Locate every Plasmodium parasite.
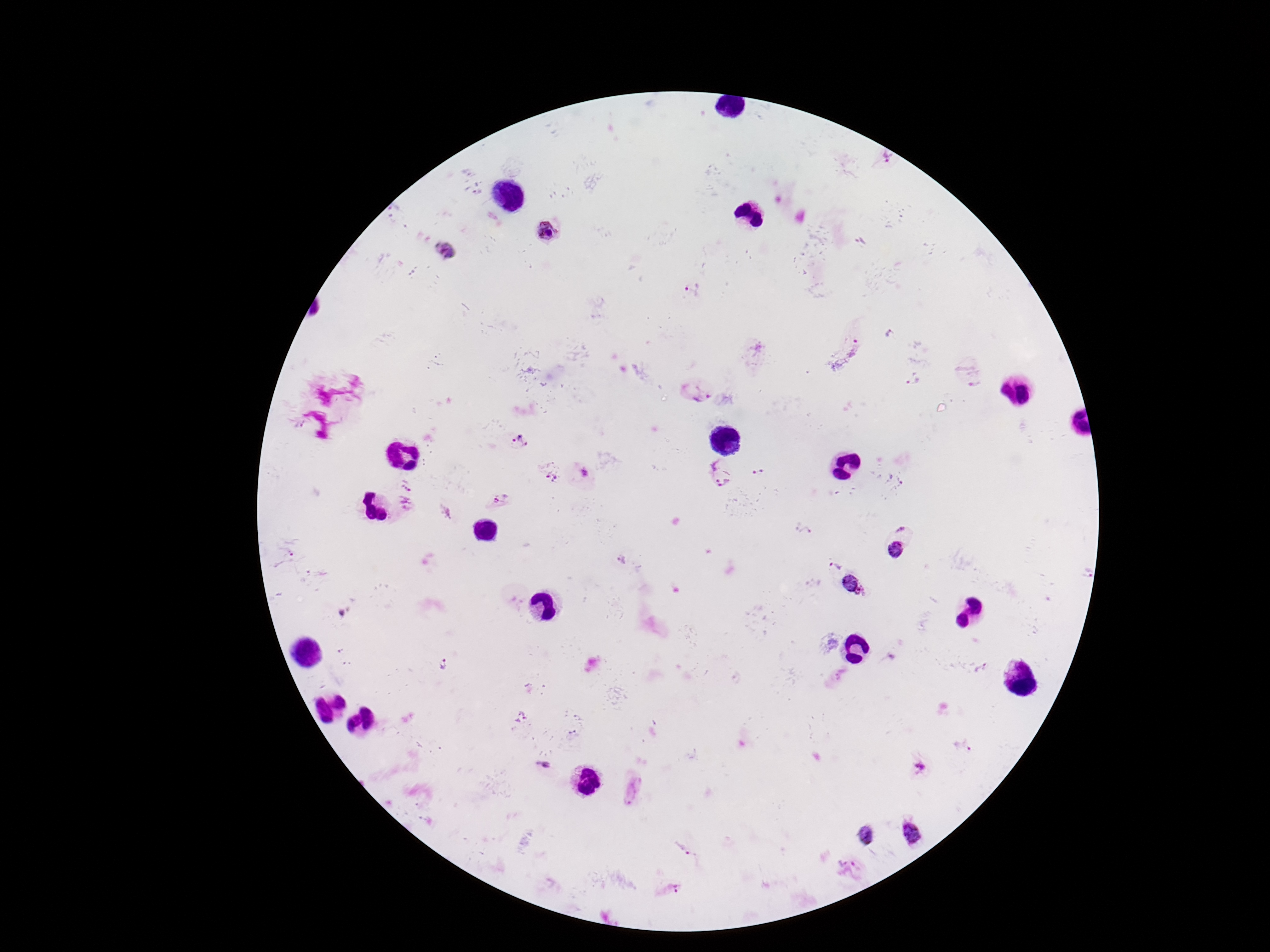
Approximate centers as {x, y} in pixels.
Plasmodium parasites: {887, 157}, {547, 232}, {445, 253}, {693, 290}, {860, 348}, {913, 380}, {700, 393}, {520, 442}, {711, 463}, {759, 470}, {553, 475}, {724, 478}, {895, 482}, {408, 485}, {500, 502}, {406, 506}, {902, 527}, {805, 531}, {895, 549}, {284, 558}, {622, 559}, {833, 565}, {854, 584}, {443, 664}, {982, 670}, {520, 716}, {963, 745}, {543, 766}, {921, 766}, {633, 788}, {912, 832}, {865, 835}, {687, 848}, {847, 860}, {673, 888}.

Image is 1270×952 pixels. Smartphone photograph taken through the microscope eyepiece. Giemsa stain. Thick blood film. 100x magnification. Patient malaria status: positive. Single field of view.